Identify the parasite.
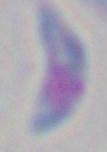

This is Toxoplasma gondii.

Summary:
  - Modality: micrograph
  - Magnification: 1000x